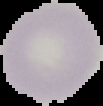
image_size: 103×106 pixels
preparation: thin blood smear
image_type: cell region segmented out of the field of view; surrounding area masked to black
result: no malaria parasites seen